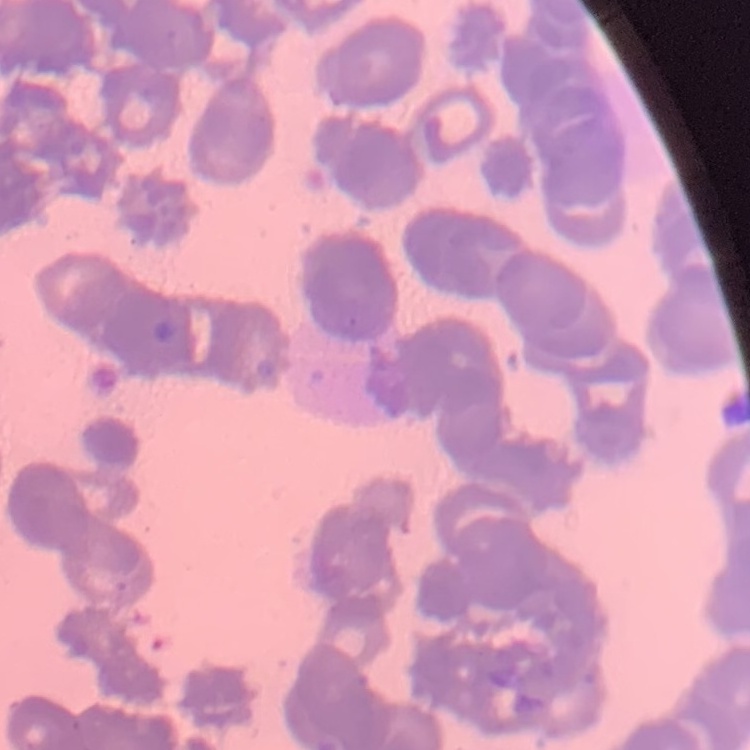

erythrocyte_morphology: rouleaux formation
preparation: thin blood film
image_type: square crop of a larger photomicrograph
stain: Field's or Giemsa